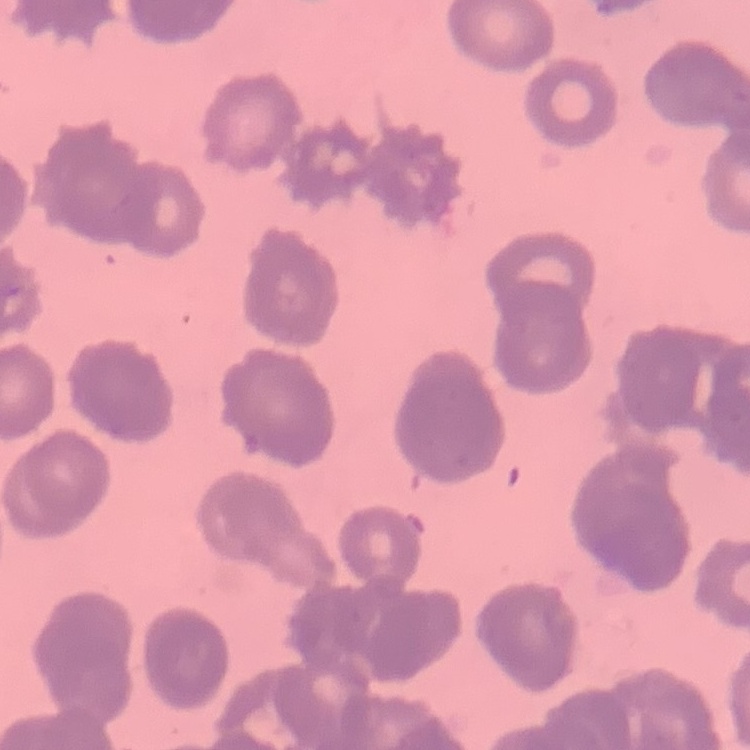
erythrocyte morphology = rouleaux formation
preparation = thin blood smear
image type = one tile cut from a larger photomicrograph
stain = Field's or Giemsa